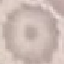
Malaria status: uninfected. Giemsa-stained preparation. Acquired by smartphone through the microscope eyepiece. Thin blood film. Cell patch, automatically extracted from a larger field of view and resized to 64 × 64 pixels.